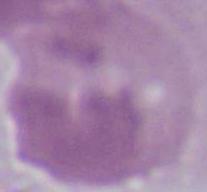

Captured at 1000x magnification. A red blood cell is seen. Micrograph.